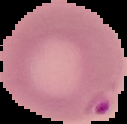

{
  "result": "malaria parasites detected",
  "preparation": "thin blood film",
  "image_type": "cell region segmented out of the field of view; surrounding area masked to black",
  "image_size": "127×124 pixels"
}